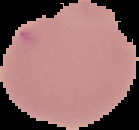
Cell region segmented out of the field of view; the surrounding area is masked to black. From a thin blood smear. Image is 139×130 pixels. Result: no Plasmodium parasites seen.